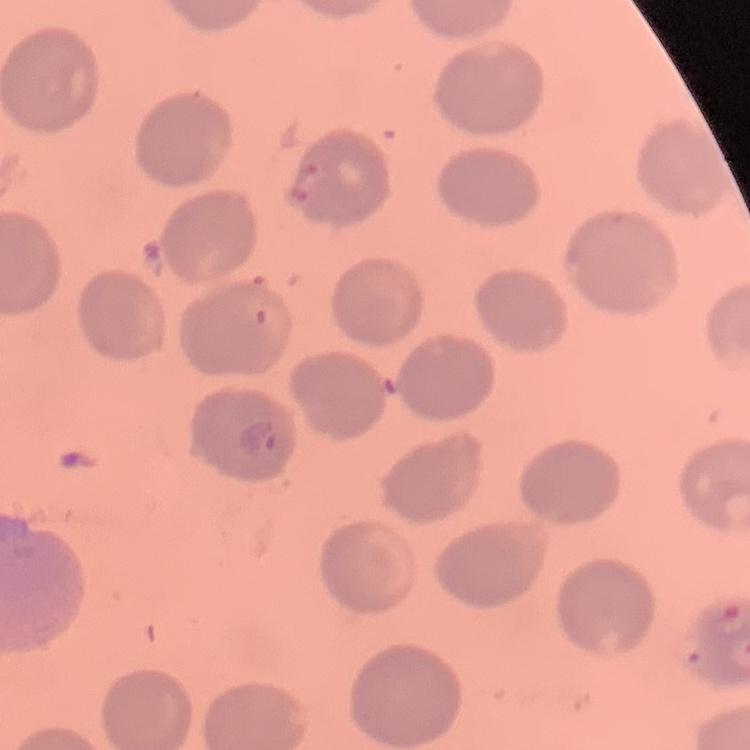 The red blood cells exhibit no rouleaux formation. Field's or Giemsa stain. Thin blood film. Square crop of a larger photomicrograph.